Classify this cell by malaria status.
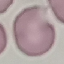

It is uninfected.

Giemsa stain. Cell patch, automatically extracted from a larger field of view and resized to 64 × 64 pixels. Thin smear of blood. Photographed with a smartphone camera at the microscope eyepiece.